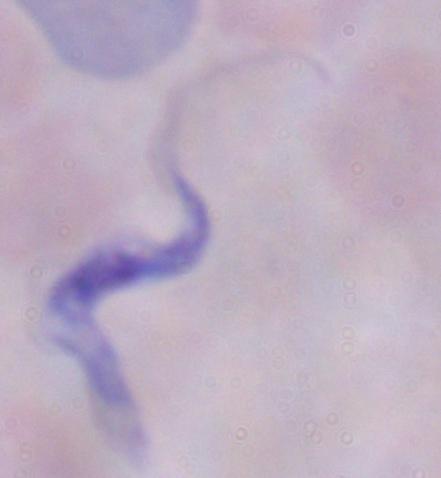
Summary:
  - Identification: trypanosome
  - Magnification: 1000x
  - Modality: micrograph